Report the malaria status of this cell.
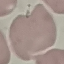
It is uninfected.

Automatically extracted cell patch, resized to 64 × 64 pixels. Thin blood smear. Giemsa-stained preparation. Acquired by smartphone through the microscope eyepiece.